Outline each Plasmodium malariae-infected red blood cell.
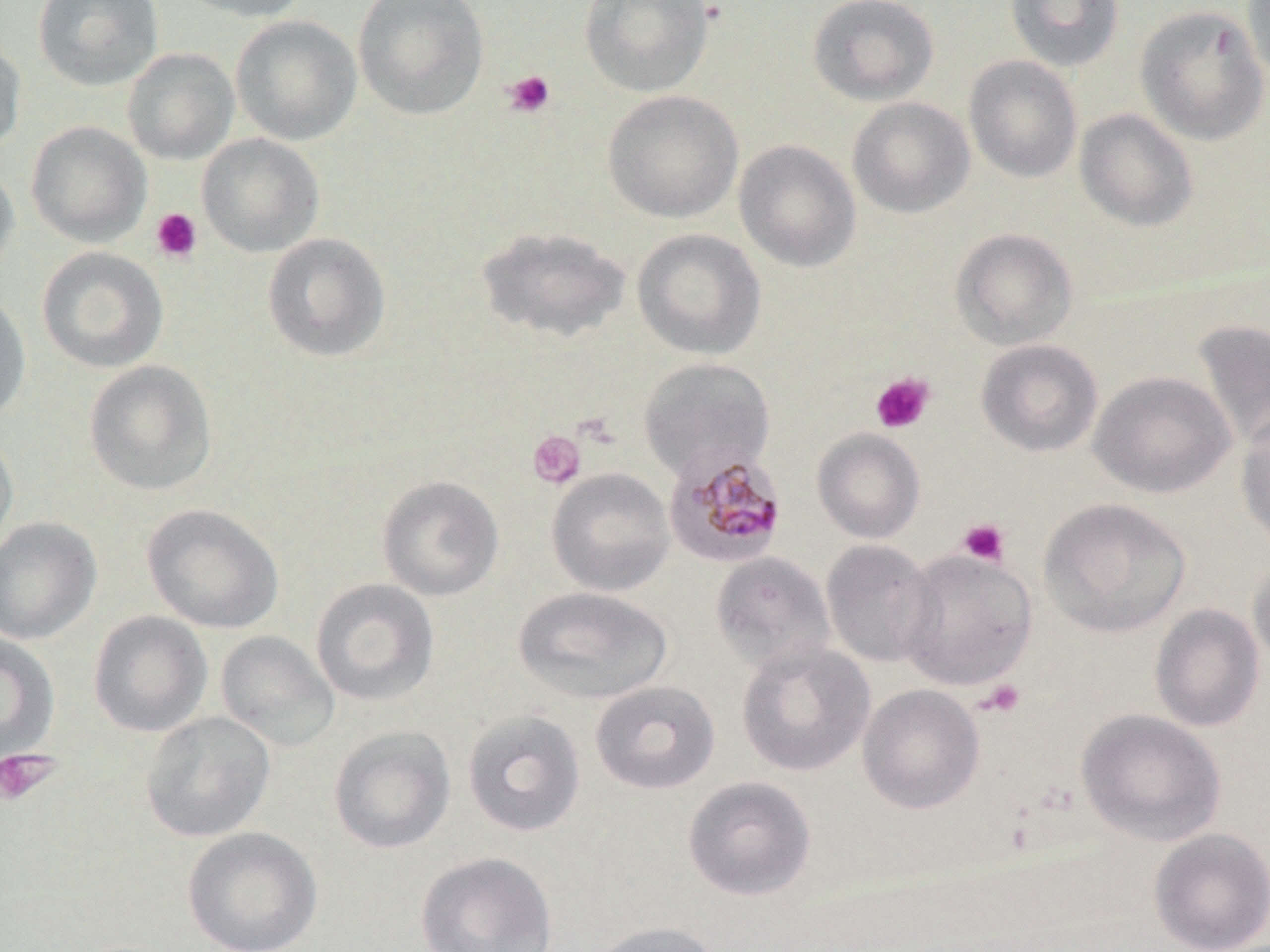

Approximate bounding boxes as (x1, y1, x2, y2) in pixels.
Plasmodium malariae-infected red blood cells: (662, 445, 788, 569).

slide_level_diagnosis: Plasmodium malariae
stain: May-Grünwald-Giemsa
platelet_locations: 'approximate bounding boxes as (x1, y1, x2, y2) in pixels: (503, 70, 555, 118), (151, 208, 202, 263), (870, 372, 935, 434), (527, 430, 586, 489), (958, 518, 1010, 566), (977, 679, 1026, 718), (0, 748, 60, 806)'
magnification: 1000x
image_size: 1270×952 pixels
modality: light microscopy
preparation: thin blood smear
uninfected_red_blood_cell_locations: 'approximate bounding boxes as (x1, y1, x2, y2) in pixels: (32, 0, 164, 90), (176, 0, 313, 22), (352, 0, 490, 120), (580, 0, 715, 98), (807, 0, 940, 107), (1005, 0, 1125, 72), (1241, 0, 1270, 85), (1135, 5, 1269, 145), (230, 14, 362, 146), (0, 36, 27, 154), (121, 47, 240, 165), (963, 55, 1083, 183), (602, 89, 743, 223), (847, 97, 975, 219), (1074, 108, 1198, 231), (26, 121, 152, 247), (196, 133, 324, 257), (734, 139, 861, 272), (0, 163, 20, 284), (475, 225, 631, 344), (632, 228, 766, 360), (950, 228, 1078, 350), (262, 232, 391, 363), (36, 246, 169, 373), (0, 291, 32, 423), (1191, 318, 1270, 455), (976, 339, 1103, 458), (638, 357, 775, 481), (84, 360, 218, 496), (1089, 370, 1236, 498), (1235, 412, 1270, 552), (812, 428, 925, 543), (0, 430, 18, 555), (546, 468, 675, 596), (376, 474, 504, 601), (1038, 497, 1191, 638), (142, 502, 284, 634), (0, 517, 102, 645), (820, 539, 939, 668), (896, 548, 1037, 691), (710, 551, 836, 674), (1248, 557, 1270, 676), (310, 578, 440, 706), (513, 586, 673, 705), (1150, 603, 1265, 732), (88, 611, 213, 737), (215, 630, 340, 752), (0, 633, 60, 764), (735, 641, 875, 777), (590, 680, 720, 794), (857, 683, 985, 814), (461, 709, 586, 837), (1076, 709, 1226, 846), (141, 711, 276, 842), (328, 725, 456, 854), (683, 776, 816, 900), (182, 826, 323, 952), (1149, 828, 1270, 951), (415, 850, 558, 952), (586, 920, 723, 952)'
field_of_view: single